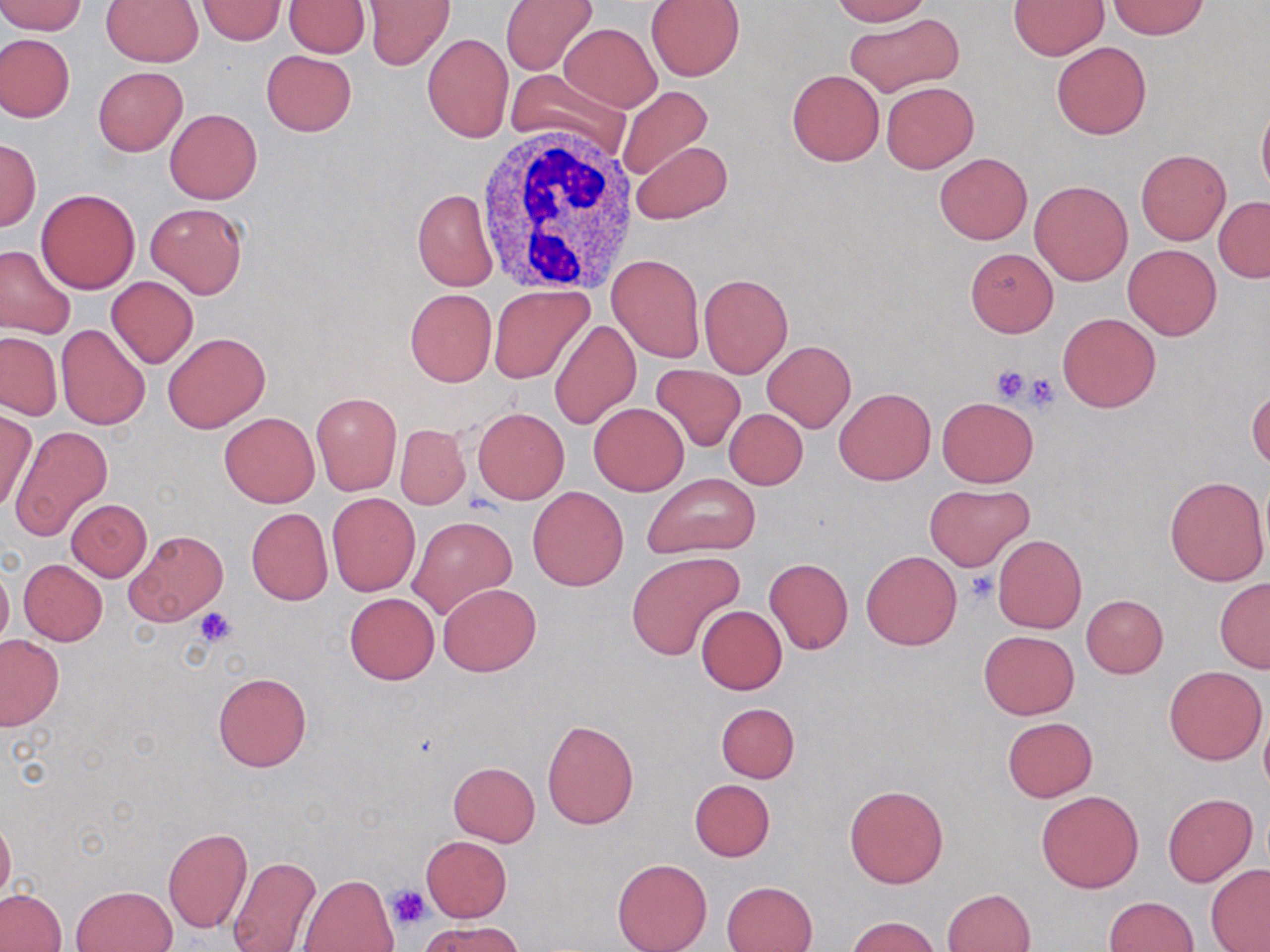
Summary:
  - Coordinate format: approximate bounding boxes as (x1, y1, x2, y2) in pixels
  - White blood cell locations: (475, 123, 645, 294)
  - Uninfected red blood cell locations: (0, 0, 88, 35), (285, 0, 370, 57), (364, 0, 454, 70), (500, 0, 597, 76), (830, 0, 932, 25), (1009, 0, 1109, 59), (101, 1, 204, 67), (198, 1, 285, 45), (645, 1, 744, 80), (1107, 1, 1210, 38), (845, 12, 963, 98), (560, 23, 661, 112), (422, 32, 513, 142), (0, 33, 75, 123), (1051, 41, 1151, 139), (261, 50, 356, 136), (93, 66, 188, 155), (507, 69, 633, 158), (787, 69, 883, 166), (881, 82, 980, 173), (615, 85, 712, 184), (1257, 98, 1270, 198), (164, 109, 263, 204), (0, 139, 40, 229), (629, 140, 730, 224), (1135, 147, 1231, 245), (934, 152, 1032, 245), (1030, 179, 1133, 286), (36, 188, 141, 294), (412, 188, 497, 290), (1214, 197, 1270, 282), (145, 203, 248, 298), (1122, 243, 1222, 340), (0, 244, 76, 338), (964, 248, 1059, 336), (608, 253, 704, 362), (698, 273, 794, 378), (106, 276, 199, 369), (489, 286, 593, 384), (405, 289, 496, 386), (1057, 312, 1160, 412), (549, 320, 640, 429), (56, 324, 150, 430), (163, 332, 270, 434), (0, 333, 61, 419), (762, 340, 855, 432), (649, 365, 746, 452), (1247, 385, 1269, 470), (834, 387, 935, 485), (312, 392, 401, 495), (937, 396, 1038, 486), (589, 402, 689, 496), (474, 407, 569, 504), (723, 408, 807, 490), (0, 409, 37, 514), (220, 411, 320, 508), (395, 424, 470, 509), (10, 427, 113, 540), (642, 472, 761, 559), (1164, 475, 1269, 587), (924, 484, 1034, 571), (528, 486, 628, 590), (327, 493, 419, 596), (66, 499, 151, 580), (246, 507, 333, 605), (408, 516, 516, 620), (127, 529, 227, 624), (992, 534, 1086, 633), (627, 551, 745, 660), (862, 551, 962, 650), (764, 557, 853, 654), (18, 558, 108, 645), (0, 561, 13, 652), (1214, 578, 1270, 674), (437, 583, 539, 676), (345, 592, 438, 684), (1082, 594, 1168, 678), (697, 605, 787, 695), (979, 629, 1078, 719), (0, 635, 64, 730), (1164, 665, 1267, 765), (213, 671, 311, 771), (716, 702, 799, 782), (1003, 717, 1096, 801), (543, 719, 639, 829), (448, 761, 541, 846), (689, 779, 776, 862), (844, 783, 949, 889), (1036, 790, 1144, 893), (1163, 792, 1257, 886), (0, 814, 15, 903), (163, 827, 253, 934), (421, 835, 511, 921), (227, 856, 323, 952), (612, 858, 711, 952), (1205, 864, 1270, 952), (298, 874, 397, 952), (722, 881, 817, 952), (69, 885, 177, 952), (943, 888, 1035, 951), (1, 889, 66, 951), (1104, 896, 1198, 951), (846, 917, 941, 952), (420, 919, 522, 951)
  - Platelet locations: (990, 364, 1035, 404), (1023, 374, 1061, 411), (965, 571, 998, 605), (194, 608, 238, 647), (387, 884, 433, 930)
  - Slide-level diagnosis: negative for blood parasites
  - Preparation: thin blood smear
  - Stain: May-Grünwald-Giemsa
  - Magnification: 1000x
  - Image size: 1270×952 pixels
  - Modality: light microscopy
  - Field of view: one of a larger specimen